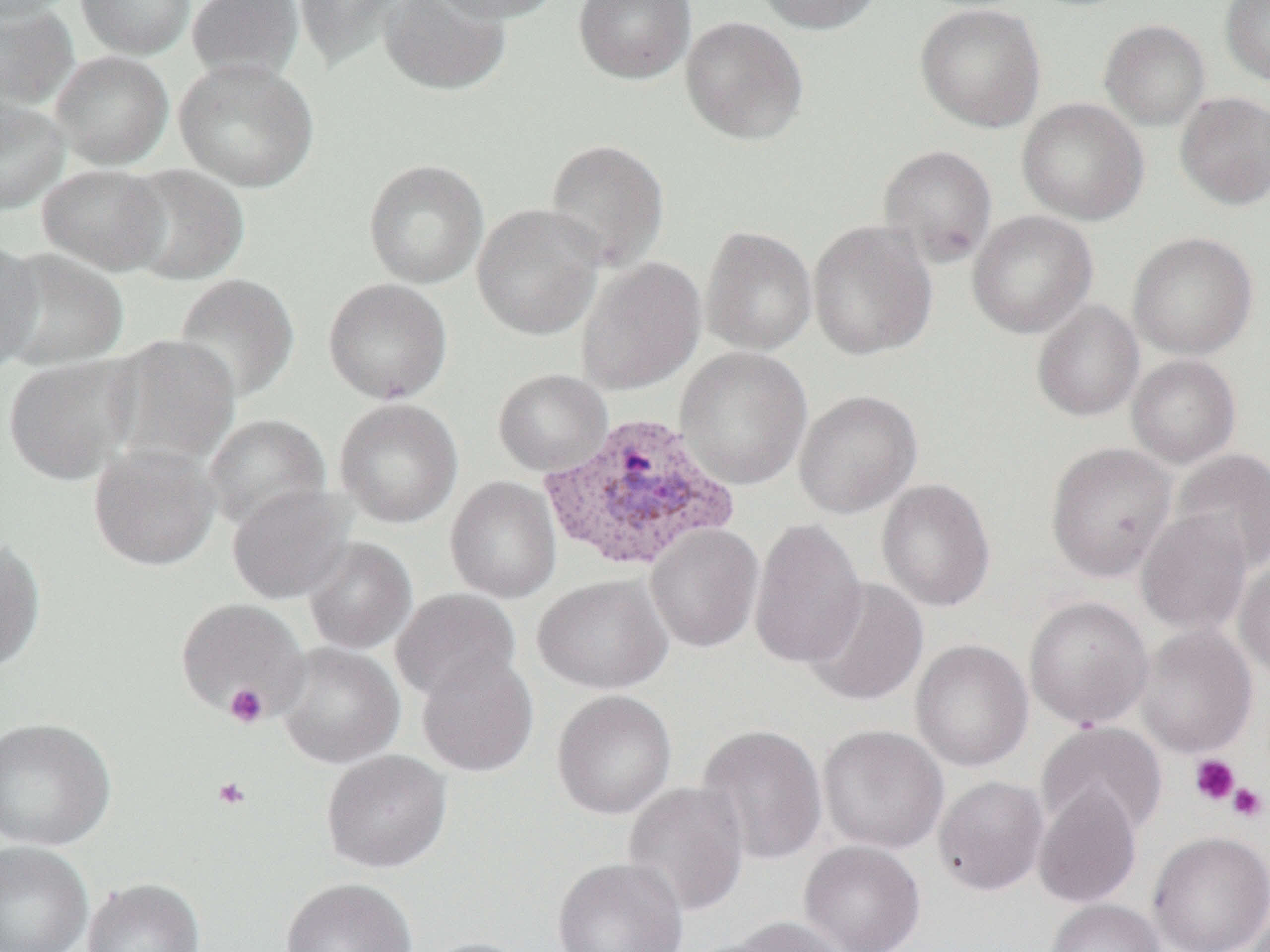
{
  "slide_level_diagnosis": "Plasmodium vivax",
  "preparation": "thin blood smear",
  "image_size": "1270×952 pixels",
  "uninfected_red_blood_cell_locations": "approximate bounding boxes as [x1, y1, x2, y2] in pixels: [0, 0, 77, 22], [75, 0, 195, 59], [186, 0, 304, 83], [293, 0, 407, 71], [379, 0, 512, 96], [426, 0, 562, 22], [573, 0, 696, 84], [755, 0, 883, 35], [1220, 0, 1270, 86], [0, 3, 80, 110], [915, 3, 1046, 133], [680, 15, 809, 146], [1099, 19, 1210, 131], [49, 50, 173, 170], [173, 58, 319, 192], [1174, 92, 1270, 211], [0, 98, 70, 214], [1017, 98, 1148, 226], [544, 138, 670, 271], [877, 144, 998, 268], [363, 158, 489, 289], [37, 163, 171, 275], [119, 164, 250, 285], [472, 204, 604, 341], [967, 210, 1098, 339], [807, 220, 937, 360], [701, 225, 818, 356], [1127, 232, 1258, 360], [0, 238, 43, 375], [0, 248, 129, 371], [576, 257, 706, 395], [173, 273, 300, 403], [323, 278, 453, 405], [1031, 300, 1144, 422], [105, 334, 241, 470], [674, 347, 812, 490], [1, 354, 139, 485], [1126, 354, 1241, 468], [492, 368, 613, 476], [793, 389, 922, 518], [335, 398, 463, 528], [203, 413, 331, 532], [88, 442, 221, 571], [1046, 442, 1176, 582], [1171, 448, 1270, 573], [445, 477, 562, 603], [876, 478, 996, 612], [227, 484, 353, 604], [1136, 510, 1253, 636], [749, 517, 868, 670], [646, 524, 764, 653], [0, 537, 47, 673], [303, 538, 417, 654], [1234, 559, 1270, 683], [532, 574, 673, 695], [802, 577, 929, 707], [391, 588, 522, 703], [1024, 595, 1153, 729], [174, 597, 310, 720], [1135, 624, 1257, 758], [910, 639, 1033, 772], [276, 643, 405, 769], [416, 654, 539, 776], [552, 690, 676, 819], [0, 716, 117, 851], [1036, 721, 1168, 839], [696, 723, 828, 866], [818, 724, 949, 854], [321, 749, 452, 872], [933, 775, 1049, 896], [622, 781, 750, 919], [1033, 783, 1142, 909], [1148, 831, 1270, 952], [799, 839, 926, 952], [0, 841, 93, 952], [552, 856, 688, 952], [82, 877, 205, 952], [280, 877, 417, 952], [1046, 898, 1165, 952], [727, 916, 853, 952], [419, 937, 538, 952]",
  "platelet_locations": "approximate bounding boxes as [x1, y1, x2, y2] in pixels: [224, 683, 269, 728], [1189, 754, 1240, 806], [213, 776, 251, 810], [1228, 783, 1268, 822]",
  "magnification": "1000x",
  "modality": "light microscopy",
  "plasmodium_vivax_infected_red_blood_cell_locations": "approximate bounding boxes as [x1, y1, x2, y2] in pixels: [539, 411, 740, 574]",
  "field_of_view": "one of a larger specimen"
}